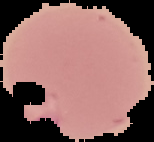

Summary:
  - Preparation: thin blood film
  - Image size: 154×142 pixels
  - Malaria status: parasitized
  - Image type: cell region segmented out of the field of view; surrounding area masked to black